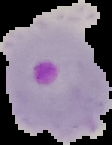
{
  "malaria_status": "parasitized",
  "image_type": "segmented cell region with the area outside set to black",
  "preparation": "thin blood smear",
  "image_size": "112×145 pixels"
}